Report the malaria status of this cell.
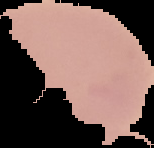
It is uninfected.

Summary:
  - Image size: 154×148 pixels
  - Preparation: thin blood smear
  - Image type: segmented cell region on a black background